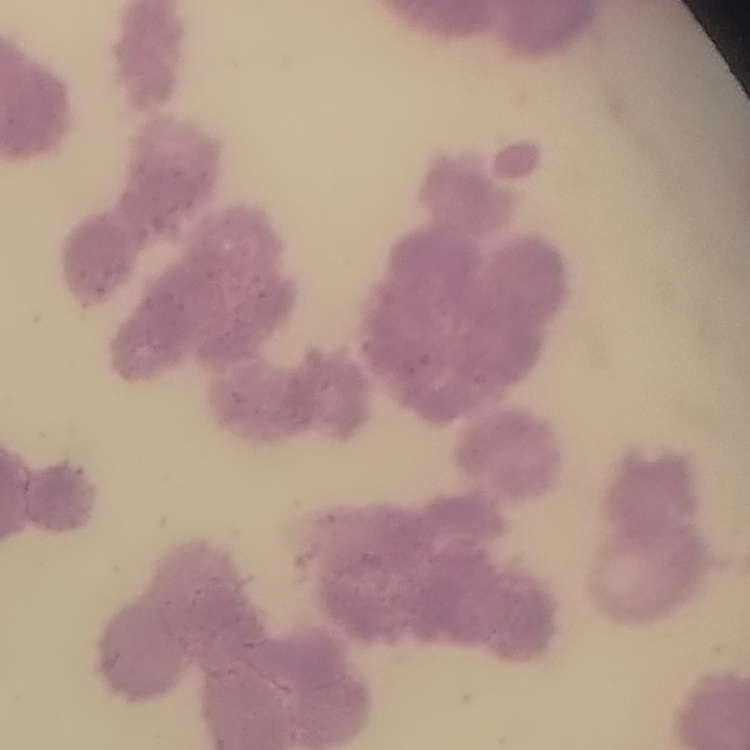 The red blood cells show rouleaux formation. One tile cut from a larger photomicrograph. Thin blood smear. Stained with either Field's or Giemsa.